Point out each leukocyte.
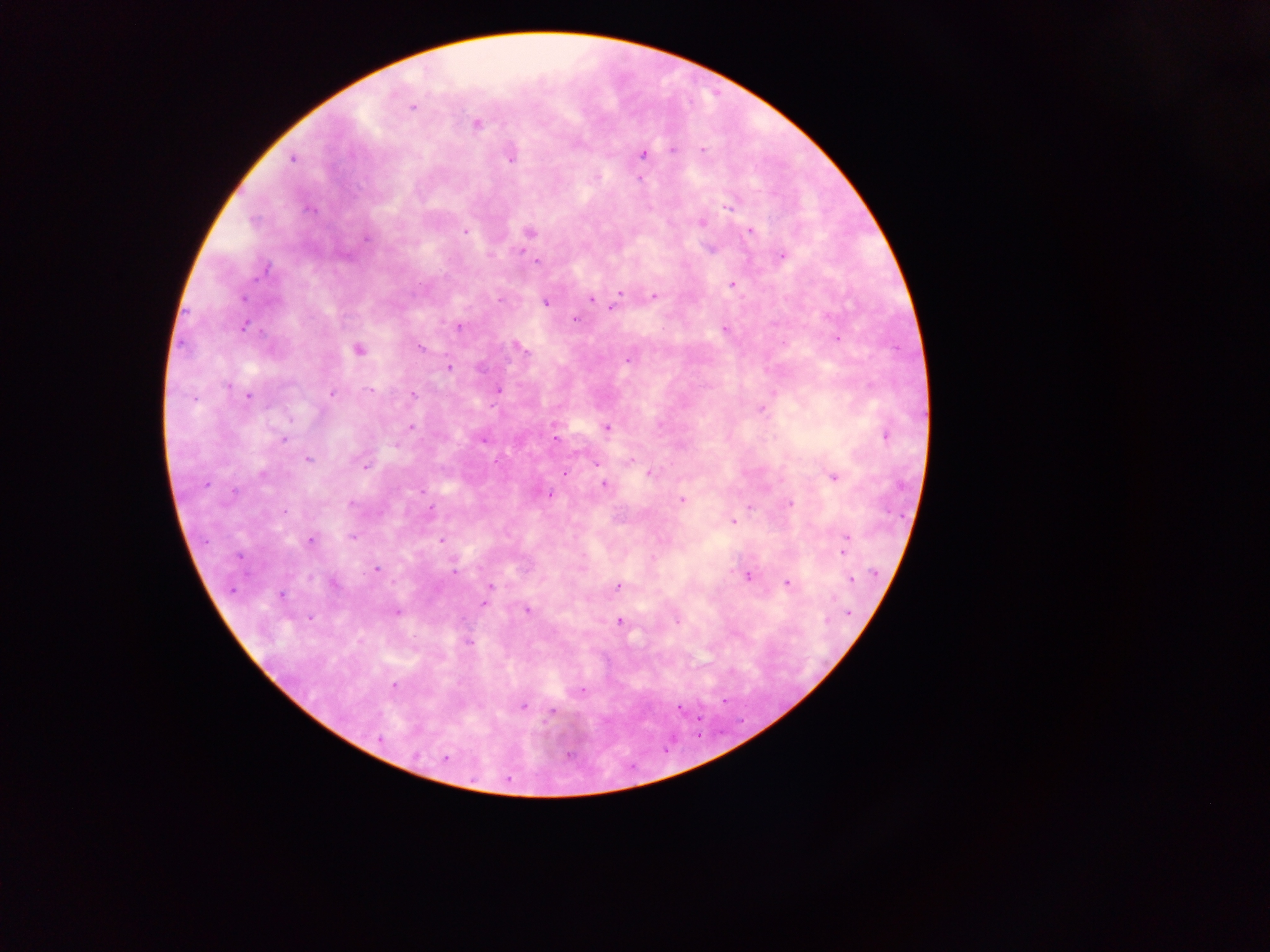

No leukocytes observed.

Approximate centers as (x, y) in pixels.
Summary:
  - Malaria parasite locations: (413, 107), (475, 123), (672, 150), (703, 151), (643, 153), (510, 155), (292, 158), (639, 179), (729, 204), (701, 222), (464, 231), (750, 231), (528, 232), (366, 236), (711, 248), (782, 255), (537, 262), (733, 283), (620, 292), (653, 296), (591, 298), (544, 302), (613, 305), (575, 319), (243, 325), (459, 327), (725, 328), (837, 338), (517, 346), (420, 348), (357, 350), (628, 358), (448, 367), (369, 390), (497, 390), (332, 391), (412, 393), (249, 395), (761, 408), (554, 424), (410, 426), (606, 427), (885, 434), (482, 438), (283, 439), (555, 439), (307, 459), (596, 462), (366, 465), (564, 472), (649, 473), (832, 476), (604, 483), (547, 493), (682, 500), (789, 503), (733, 520), (352, 536), (846, 536), (310, 540), (441, 540), (842, 552), (652, 559), (376, 569), (747, 575), (850, 580), (331, 582), (786, 582), (618, 585), (490, 586), (281, 594), (484, 602), (526, 610), (397, 612), (847, 613), (676, 619), (619, 621), (468, 641), (393, 685), (522, 706), (679, 708), (551, 711), (445, 759)
  - Image size: 1270×952 pixels
  - Country: Ghana
  - Field of view: single
  - Capture: mobile-phone photograph through a microscope
  - Preparation: thick blood smear